Classify this cell by malaria status.
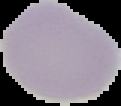
It is uninfected.

image_size: 121×106 pixels
image_type: segmented cell region on a black background
preparation: thin blood smear